Report the malaria status of this cell.
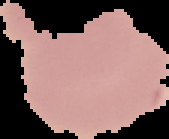

Uninfected.

image_type: segmented cell region on a black background
image_size: 169×139 pixels
preparation: thin blood smear